Name the parasite shown.
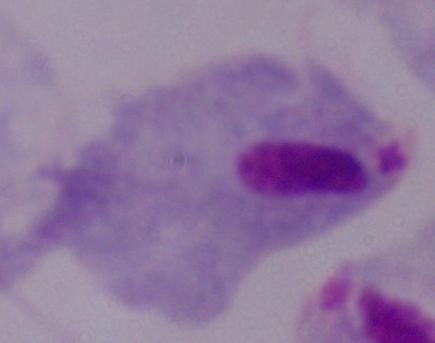
A trichomonad.

Captured at 1000x magnification. Photomicrograph.